Assess the morphology of the red blood cells.
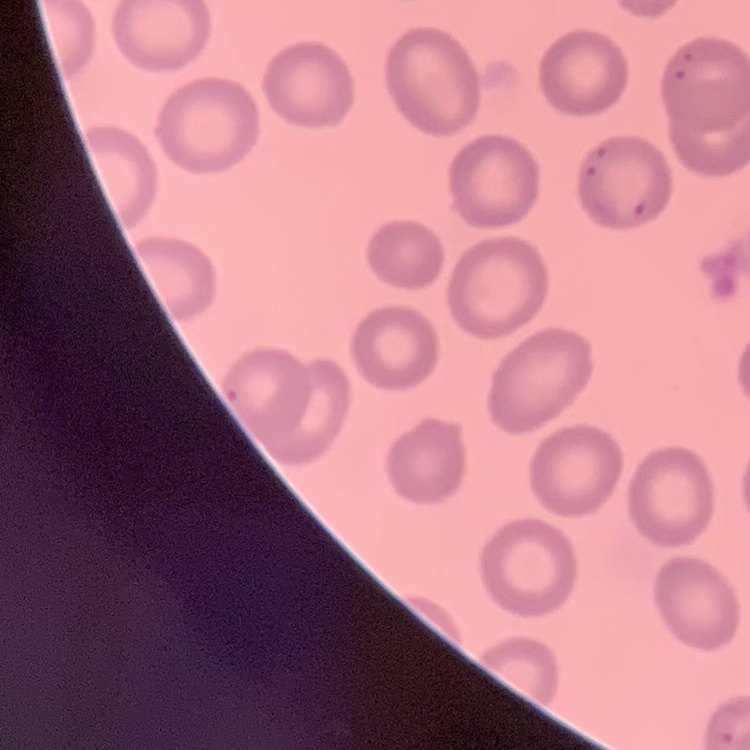

No rouleaux formation.

{
  "stain": "Field's or Giemsa",
  "preparation": "thin blood film",
  "image_type": "square crop of a larger photomicrograph"
}